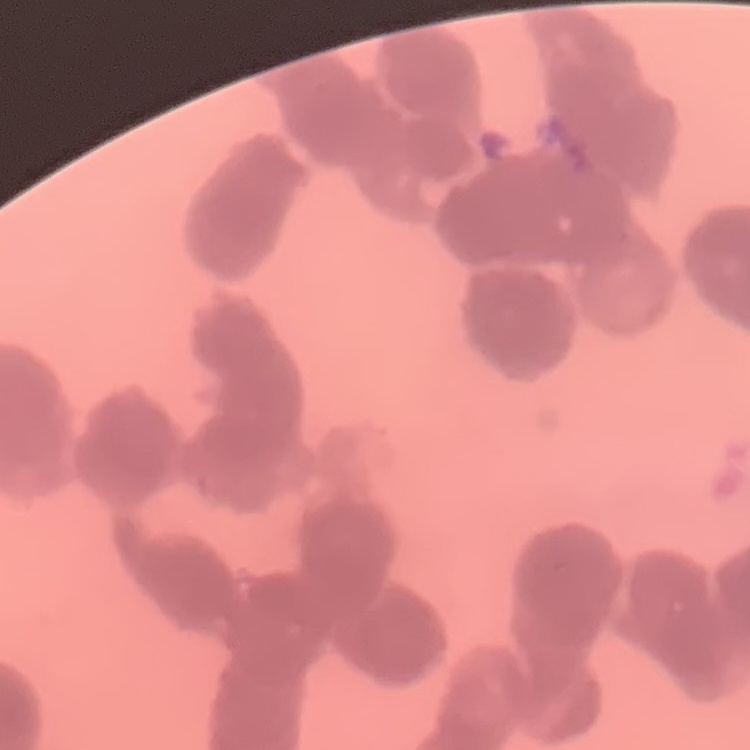
red blood cell morphology = rouleaux formation
image type = one tile cut from a larger photomicrograph
preparation = thin blood film
stain = Field's or Giemsa